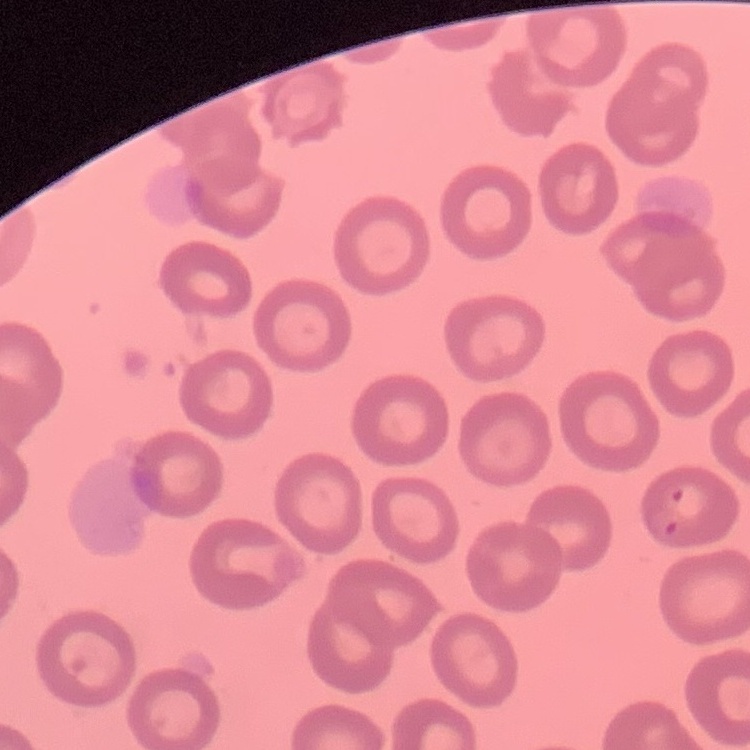
erythrocyte_morphology: no rouleaux formation
preparation: thin peripheral smear
image_type: square crop of a larger photomicrograph
stain: Field's or Giemsa